Classify this cell by malaria status.
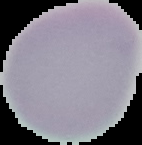

It is uninfected.

Summary:
  - Image size: 142×145 pixels
  - Image type: segmented cell region with the area outside set to black
  - Preparation: thin blood smear